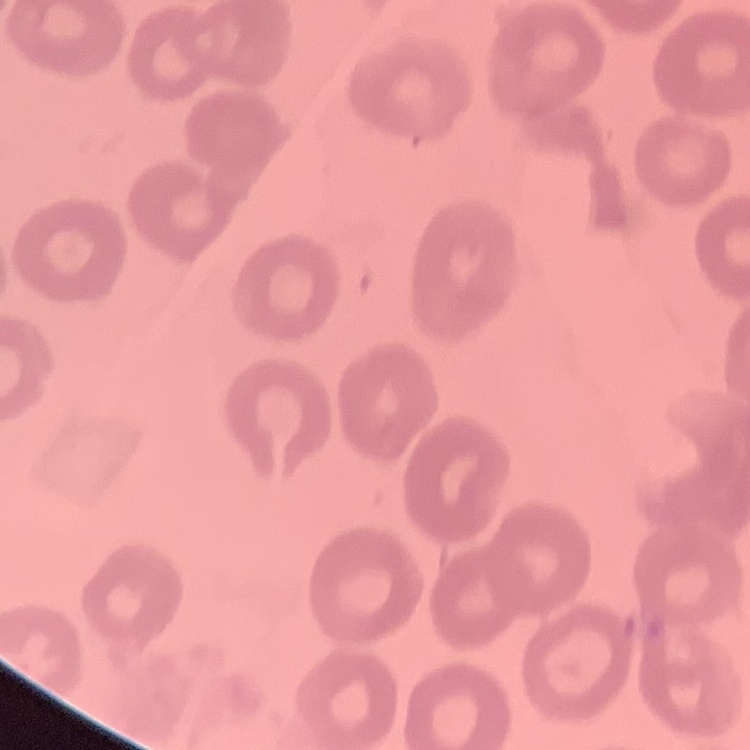 The red blood cells exhibit no rouleaux formation. Square crop of a larger photomicrograph. Stained with either Field's or Giemsa. Thin peripheral smear.